Classify this cell by malaria status.
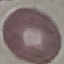
It is uninfected.

Giemsa-stained preparation. Photographed with a smartphone camera at the microscope eyepiece. Cell patch, automatically extracted from a larger field of view and resized to 64 × 64 pixels. Thin blood film.